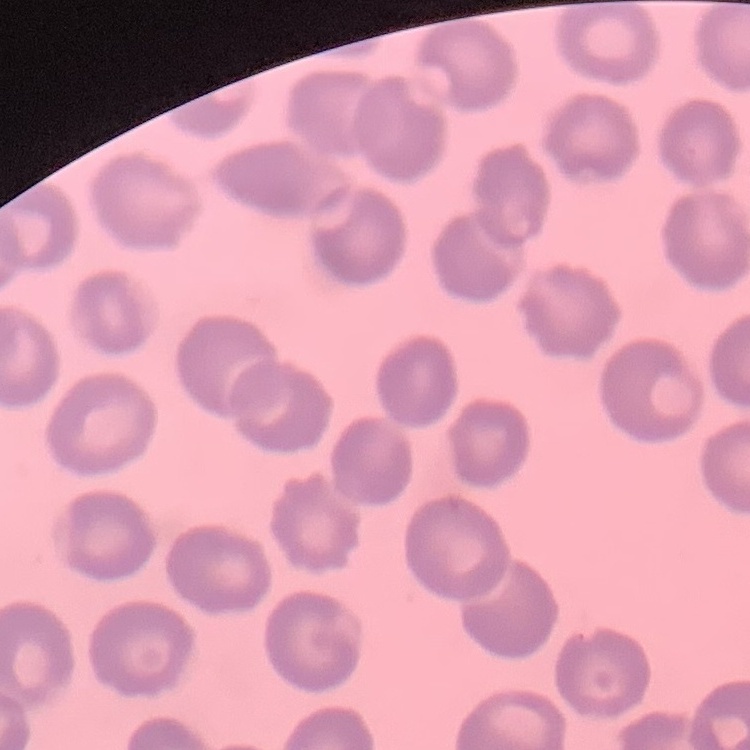

Summary:
  - Erythrocyte morphology: no rouleaux formation
  - Preparation: thin blood smear
  - Image type: square crop of a larger photomicrograph
  - Stain: Field's or Giemsa